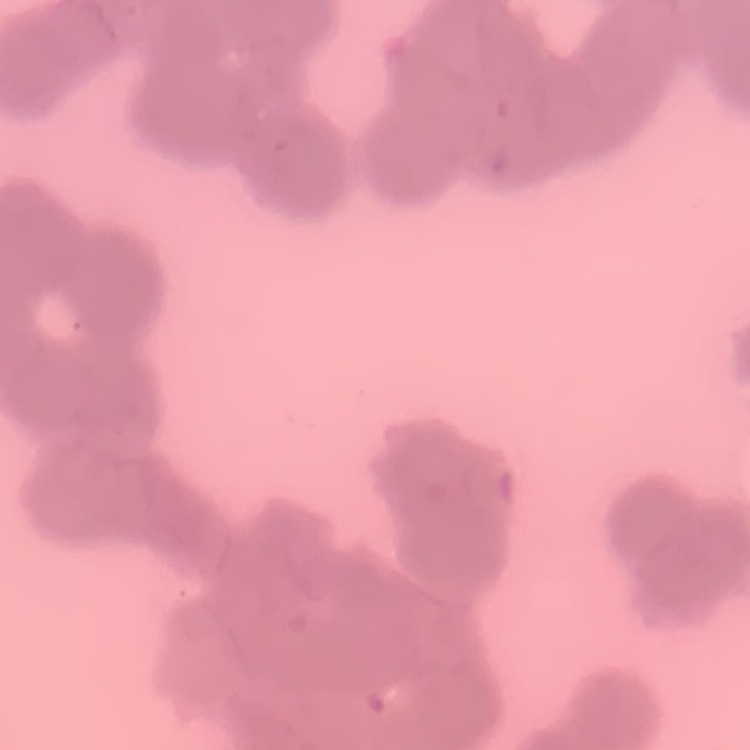
Summary:
  - Erythrocyte morphology: rouleaux formation
  - Image type: square crop of a larger photomicrograph
  - Stain: Field's or Giemsa
  - Preparation: thin blood smear